State which cell type is depicted.
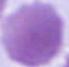
An erythrocyte.

Micrograph. Captured at 1000x magnification.